Describe the morphology of the red blood cells.
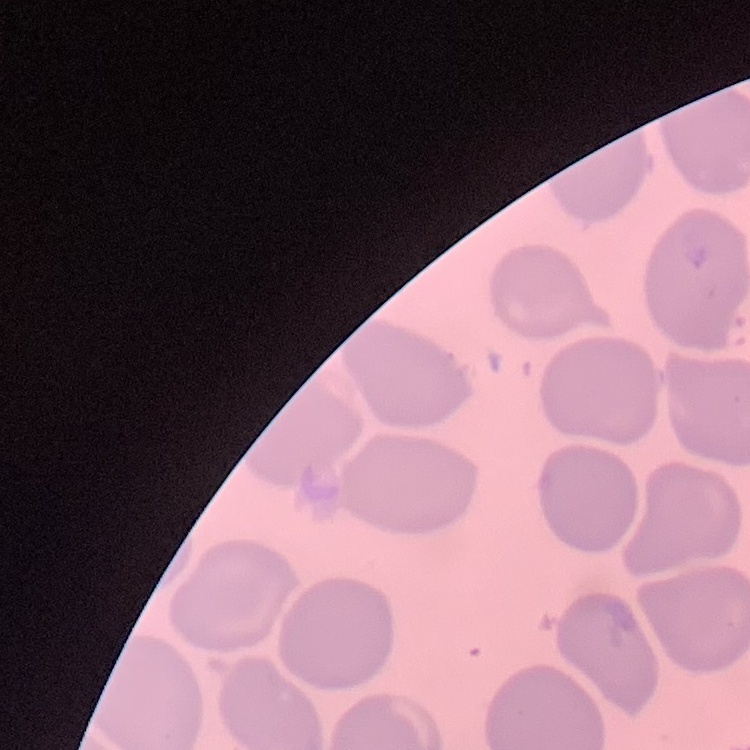

No rouleaux formation.

stain = Field's or Giemsa
preparation = thin blood smear
image type = one tile cut from a larger photomicrograph